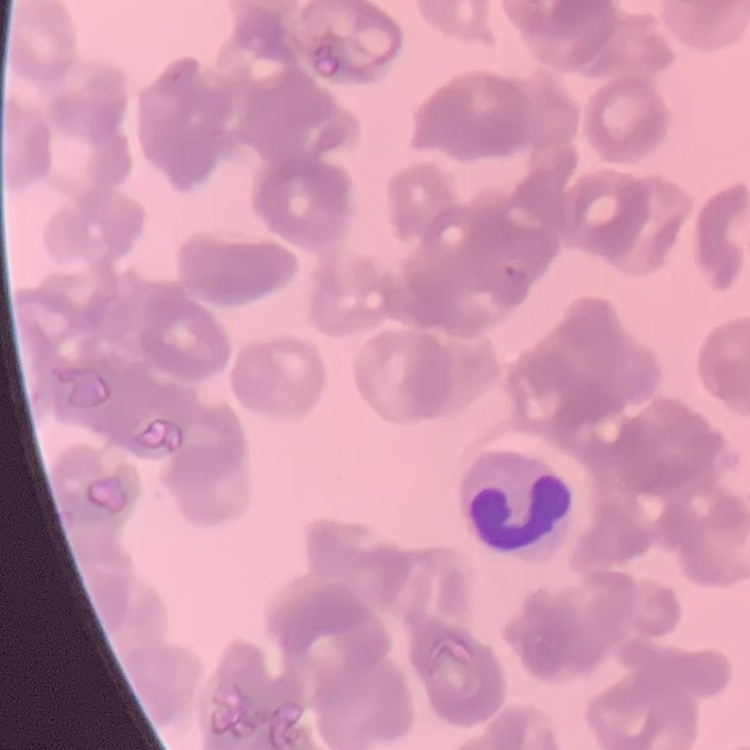

red_blood_cell_morphology: rouleaux formation
image_type: one tile cut from a larger photomicrograph
preparation: thin peripheral smear
stain: Field's or Giemsa